Give the position of every malaria parasite.
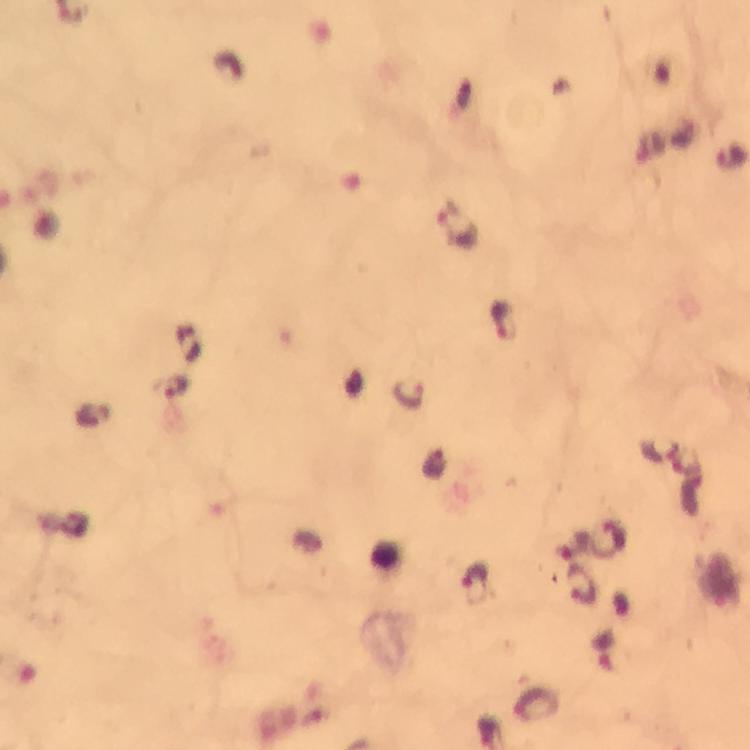
Approximate centers as [x, y] in pixels.
Malaria parasites: [731, 157], [457, 228], [501, 320], [176, 386], [409, 391], [475, 582].

image size = 750×750 pixels
cropped from = a single field of view
immersion oil = used
context = from a diagnostic examination for malaria
capture = smartphone mounted on the microscope
preparation = thick blood film
magnification = 100x
stain = Giemsa